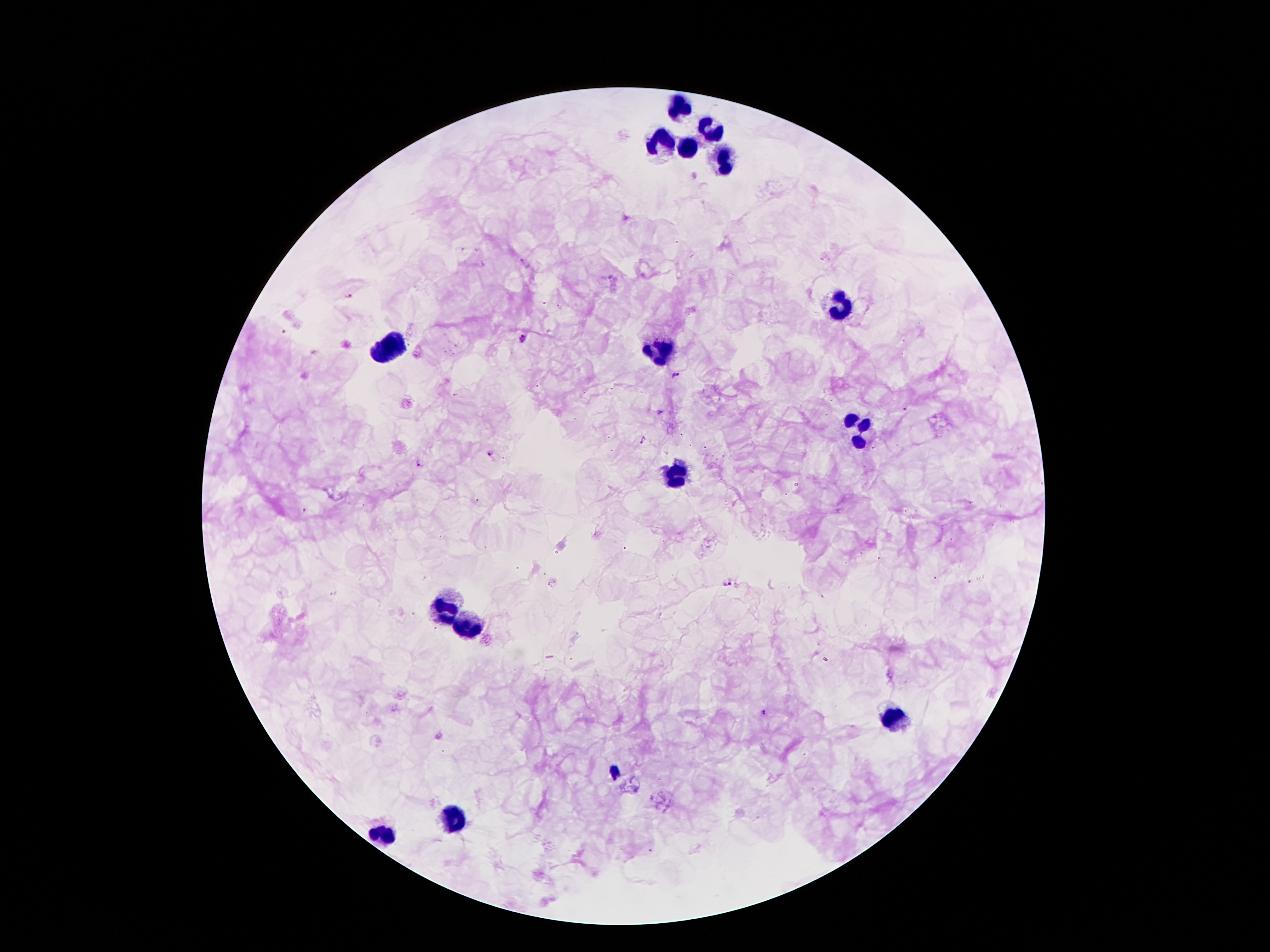

Approximate centers as (x, y) in pixels.
Summary:
  - Leukocyte locations: (680, 107), (710, 129), (662, 139), (684, 149), (720, 159), (842, 305), (390, 346), (664, 350), (854, 426), (674, 474), (448, 608), (472, 624), (898, 720), (454, 816), (384, 836)
  - Malaria parasite locations: (349, 296), (521, 337), (676, 375), (660, 411), (643, 441), (490, 453), (418, 462), (726, 581), (763, 711), (616, 773)
  - Capture: smartphone through the microscope eyepiece
  - Patient malaria status: infected with Plasmodium falciparum
  - Image size: 1270×952 pixels
  - Preparation: thick blood film
  - Stain: Giemsa
  - Magnification: 100x
  - Field of view: single